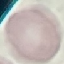
Summary:
  - Result: negative for malaria parasites
  - Stain: Giemsa
  - Capture: smartphone camera at the microscope eyepiece
  - Image type: cell patch, automatically extracted from a larger field of view and resized to 64 × 64 pixels
  - Preparation: thin blood film